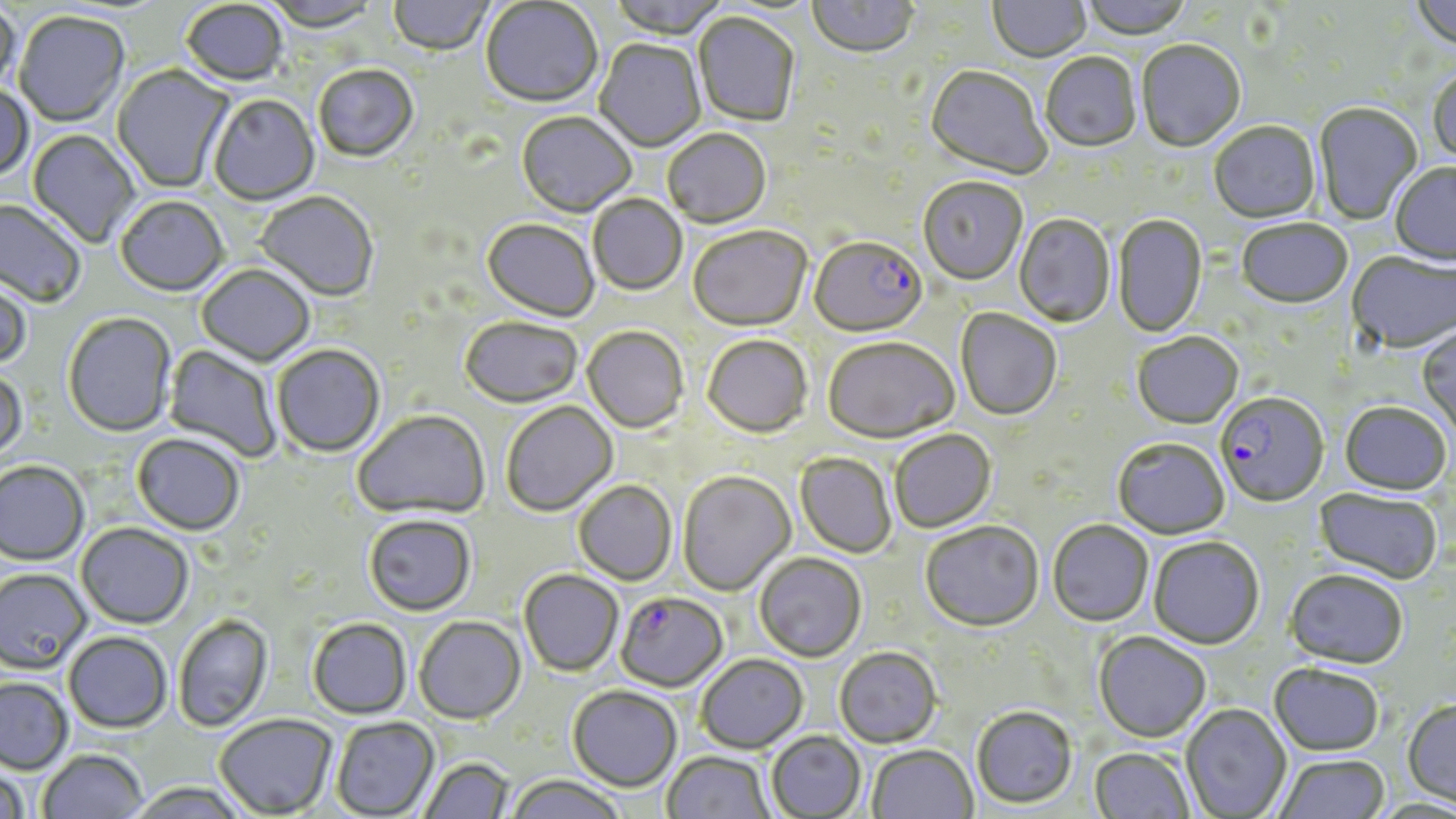

Approximate bounding boxes as (x1,y1)-(x2,y2) corner pairs in pixels. Uninfected red blood cell locations: (261,0)-(382,34), (608,0)-(728,41), (808,0)-(920,61), (1077,0)-(1194,42), (1410,0)-(1456,53), (388,1)-(495,57), (481,1)-(603,110), (988,1)-(1091,64), (0,2)-(21,98), (181,2)-(288,88), (14,13)-(130,128), (693,14)-(800,128), (594,40)-(706,153), (1136,41)-(1246,154), (1041,54)-(1142,154), (112,65)-(234,194), (314,66)-(419,164), (924,67)-(1051,181), (1428,67)-(1456,169), (0,86)-(33,184), (208,96)-(319,207), (1313,103)-(1423,227), (516,113)-(636,219), (1209,123)-(1321,226), (27,130)-(139,248), (663,130)-(771,230), (1390,164)-(1456,267), (918,179)-(1027,287), (254,192)-(379,303), (588,195)-(687,296), (116,198)-(228,298), (0,199)-(86,308), (1013,215)-(1116,328), (1113,216)-(1207,339), (482,220)-(599,324), (1236,220)-(1353,311), (688,227)-(812,333), (1347,254)-(1456,355), (196,265)-(315,367), (0,274)-(32,370), (955,309)-(1061,421), (63,313)-(177,437), (460,319)-(582,409), (1417,326)-(1456,437), (582,327)-(689,434), (1132,334)-(1244,431), (702,336)-(813,439), (823,340)-(959,445), (163,344)-(281,463), (272,345)-(385,457), (0,368)-(27,461), (501,402)-(618,517), (1339,403)-(1451,498), (353,410)-(490,520), (890,430)-(996,533), (132,433)-(245,536), (1113,439)-(1230,541), (795,454)-(897,558), (0,461)-(89,566), (677,472)-(796,597), (573,481)-(677,586), (1313,489)-(1442,586), (364,515)-(476,616), (1047,521)-(1154,628), (920,522)-(1044,634), (76,523)-(194,629), (1148,538)-(1265,651), (754,554)-(866,662), (0,568)-(91,673), (518,570)-(624,677), (1284,572)-(1408,671), (173,615)-(273,732), (414,617)-(526,725), (307,619)-(412,720), (63,632)-(172,733), (1093,633)-(1211,744), (835,648)-(941,748), (696,654)-(809,754), (1269,665)-(1384,758), (0,677)-(73,774), (567,686)-(682,792), (1402,700)-(1456,808), (1181,705)-(1292,818), (971,707)-(1077,809), (214,714)-(338,817), (331,717)-(439,818), (766,730)-(866,817), (866,745)-(977,819), (1088,748)-(1194,819), (37,749)-(148,818), (662,751)-(774,819), (1274,755)-(1392,819), (420,757)-(514,819), (0,765)-(30,819), (506,775)-(625,819), (125,782)-(251,819). Plasmodium falciparum-infected red blood cell locations: (809,239)-(927,340), (1215,394)-(1330,509), (615,592)-(728,692). Slide-level diagnosis: Plasmodium falciparum. Image is 1456×819 pixels. Captured at 1000x magnification. Single field of view. Optical microscopy. Thin blood smear. May-Grünwald-Giemsa-stained preparation.